Locate every blood parasite and identify its species.
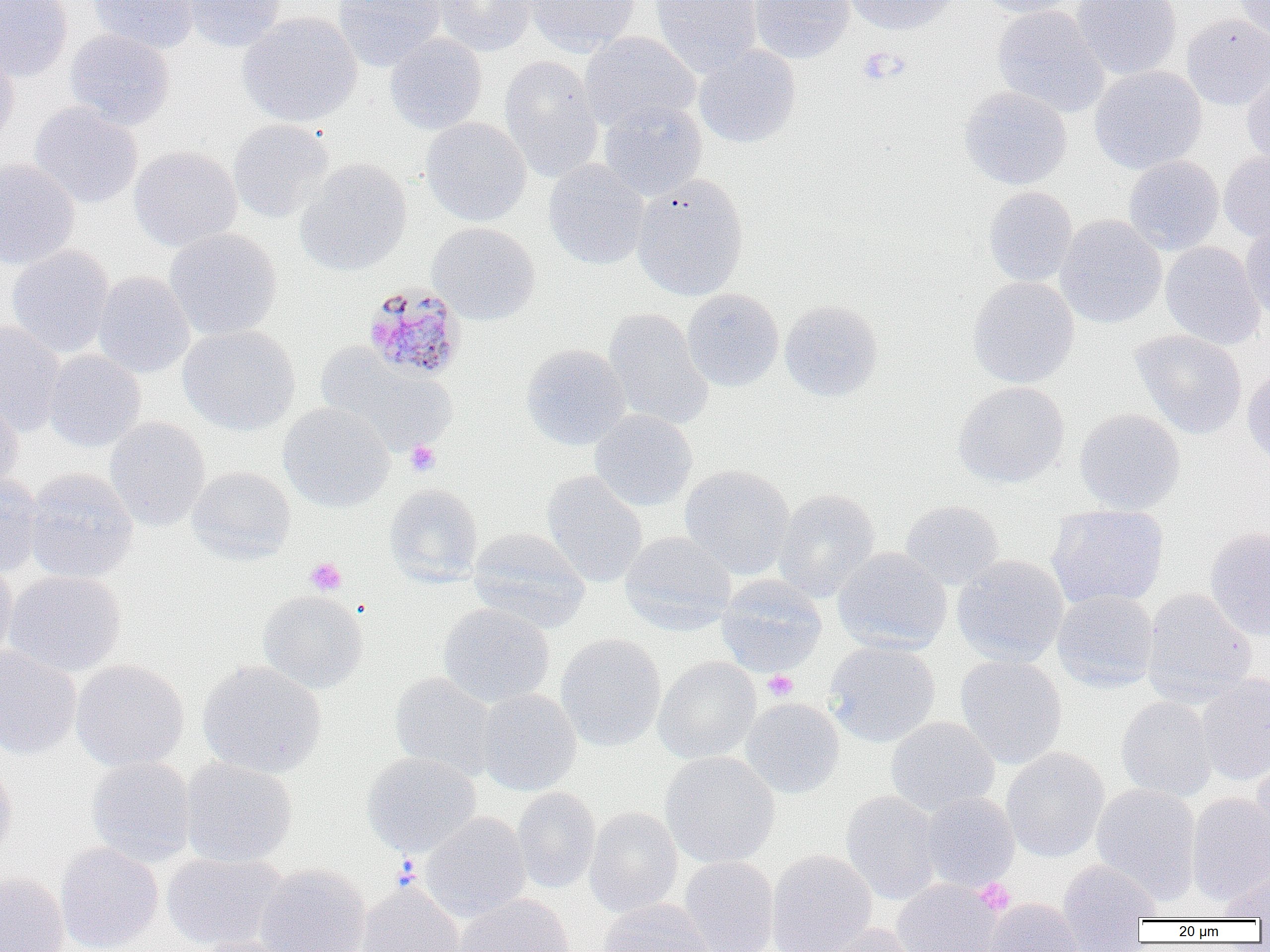
Approximate bounding boxes as named x1/y1/x2/y2 corners in pixels.
Plasmodium malariae-infected red blood cells: (x1=361, y1=284, x2=468, y2=382).
No Plasmodium falciparum, Plasmodium ovale, Plasmodium vivax, Babesia divergens, or Trypanosoma brucei observed.

Summary:
  - Uninfected red blood cell locations (subset): (x1=0, y1=0, x2=73, y2=82), (x1=89, y1=0, x2=199, y2=54), (x1=182, y1=0, x2=286, y2=52), (x1=333, y1=0, x2=445, y2=71), (x1=433, y1=0, x2=538, y2=57), (x1=525, y1=0, x2=641, y2=56), (x1=650, y1=0, x2=762, y2=78), (x1=748, y1=0, x2=855, y2=63), (x1=841, y1=0, x2=960, y2=35), (x1=977, y1=0, x2=1081, y2=18), (x1=1072, y1=0, x2=1182, y2=80), (x1=1233, y1=0, x2=1270, y2=44), (x1=992, y1=4, x2=1110, y2=118), (x1=237, y1=12, x2=362, y2=127), (x1=1181, y1=14, x2=1270, y2=111), (x1=65, y1=30, x2=175, y2=130), (x1=579, y1=31, x2=700, y2=132), (x1=384, y1=33, x2=487, y2=135), (x1=693, y1=44, x2=801, y2=148), (x1=0, y1=46, x2=19, y2=152), (x1=499, y1=55, x2=604, y2=181), (x1=1089, y1=65, x2=1207, y2=173), (x1=1241, y1=66, x2=1270, y2=169), (x1=959, y1=85, x2=1072, y2=190), (x1=598, y1=101, x2=707, y2=200), (x1=30, y1=102, x2=143, y2=208), (x1=420, y1=116, x2=531, y2=226), (x1=227, y1=119, x2=334, y2=223), (x1=129, y1=146, x2=242, y2=251), (x1=1219, y1=149, x2=1270, y2=243), (x1=1123, y1=155, x2=1224, y2=255), (x1=0, y1=158, x2=80, y2=269), (x1=295, y1=158, x2=412, y2=276), (x1=543, y1=159, x2=649, y2=270), (x1=631, y1=174, x2=749, y2=300), (x1=983, y1=186, x2=1078, y2=286), (x1=1055, y1=215, x2=1166, y2=329), (x1=1240, y1=221, x2=1270, y2=322), (x1=427, y1=222, x2=540, y2=325), (x1=164, y1=228, x2=283, y2=341), (x1=1160, y1=242, x2=1265, y2=350), (x1=7, y1=244, x2=115, y2=357), (x1=92, y1=271, x2=195, y2=378), (x1=967, y1=276, x2=1080, y2=389), (x1=681, y1=288, x2=784, y2=392), (x1=779, y1=300, x2=883, y2=402), (x1=603, y1=309, x2=713, y2=430), (x1=0, y1=320, x2=67, y2=436), (x1=178, y1=325, x2=300, y2=435), (x1=1130, y1=329, x2=1247, y2=439), (x1=521, y1=344, x2=631, y2=451), (x1=316, y1=345, x2=456, y2=457), (x1=43, y1=350, x2=145, y2=452), (x1=1242, y1=361, x2=1270, y2=468), (x1=952, y1=381, x2=1070, y2=488), (x1=0, y1=393, x2=24, y2=492), (x1=278, y1=402, x2=395, y2=512), (x1=1074, y1=408, x2=1185, y2=515), (x1=590, y1=409, x2=697, y2=511), (x1=105, y1=417, x2=210, y2=532), (x1=680, y1=464, x2=795, y2=580), (x1=187, y1=466, x2=295, y2=564), (x1=24, y1=468, x2=138, y2=584), (x1=541, y1=470, x2=647, y2=588), (x1=0, y1=471, x2=43, y2=577), (x1=383, y1=483, x2=484, y2=586), (x1=773, y1=489, x2=880, y2=602), (x1=900, y1=500, x2=1005, y2=590), (x1=1046, y1=505, x2=1169, y2=611), (x1=468, y1=527, x2=590, y2=632), (x1=1205, y1=527, x2=1270, y2=641), (x1=619, y1=531, x2=736, y2=636), (x1=832, y1=547, x2=952, y2=654), (x1=952, y1=555, x2=1068, y2=666), (x1=0, y1=561, x2=16, y2=667), (x1=4, y1=570, x2=127, y2=677), (x1=716, y1=574, x2=827, y2=676), (x1=257, y1=589, x2=368, y2=693), (x1=1141, y1=589, x2=1257, y2=707), (x1=1052, y1=590, x2=1159, y2=693), (x1=438, y1=603, x2=555, y2=707), (x1=556, y1=633, x2=666, y2=751), (x1=824, y1=639, x2=941, y2=748), (x1=0, y1=646, x2=82, y2=760), (x1=955, y1=654, x2=1067, y2=769), (x1=653, y1=656, x2=761, y2=764), (x1=70, y1=659, x2=190, y2=772), (x1=197, y1=660, x2=326, y2=779), (x1=390, y1=672, x2=498, y2=779), (x1=1195, y1=673, x2=1270, y2=786), (x1=476, y1=689, x2=581, y2=796), (x1=1116, y1=696, x2=1217, y2=802), (x1=740, y1=698, x2=844, y2=799), (x1=885, y1=716, x2=999, y2=816), (x1=1001, y1=746, x2=1109, y2=863), (x1=660, y1=751, x2=780, y2=868), (x1=361, y1=752, x2=481, y2=858), (x1=0, y1=754, x2=17, y2=864), (x1=87, y1=756, x2=196, y2=866), (x1=178, y1=757, x2=297, y2=867), (x1=1252, y1=758, x2=1270, y2=859), (x1=1091, y1=783, x2=1201, y2=905), (x1=512, y1=787, x2=601, y2=893), (x1=841, y1=790, x2=943, y2=905), (x1=1186, y1=792, x2=1270, y2=907), (x1=919, y1=793, x2=1020, y2=892), (x1=583, y1=806, x2=683, y2=918), (x1=420, y1=812, x2=531, y2=922), (x1=55, y1=842, x2=163, y2=952), (x1=767, y1=849, x2=877, y2=952), (x1=161, y1=852, x2=286, y2=951), (x1=678, y1=856, x2=779, y2=952), (x1=1057, y1=859, x2=1160, y2=949), (x1=255, y1=864, x2=371, y2=952), (x1=1213, y1=870, x2=1270, y2=922), (x1=0, y1=871, x2=69, y2=952), (x1=355, y1=882, x2=464, y2=952), (x1=453, y1=893, x2=575, y2=952), (x1=982, y1=897, x2=1085, y2=952), (x1=596, y1=898, x2=713, y2=952), (x1=811, y1=922, x2=925, y2=952), (x1=193, y1=935, x2=302, y2=952)
  - Platelet locations (subset): (x1=858, y1=48, x2=906, y2=86), (x1=404, y1=440, x2=441, y2=477), (x1=305, y1=557, x2=347, y2=595), (x1=762, y1=671, x2=798, y2=701), (x1=974, y1=878, x2=1015, y2=916)
  - Slide-level diagnosis: Plasmodium malariae
  - Magnification: 1000x
  - Modality: light microscopy
  - Field of view: single
  - Preparation: thin blood smear
  - Image size: 1270×952 pixels